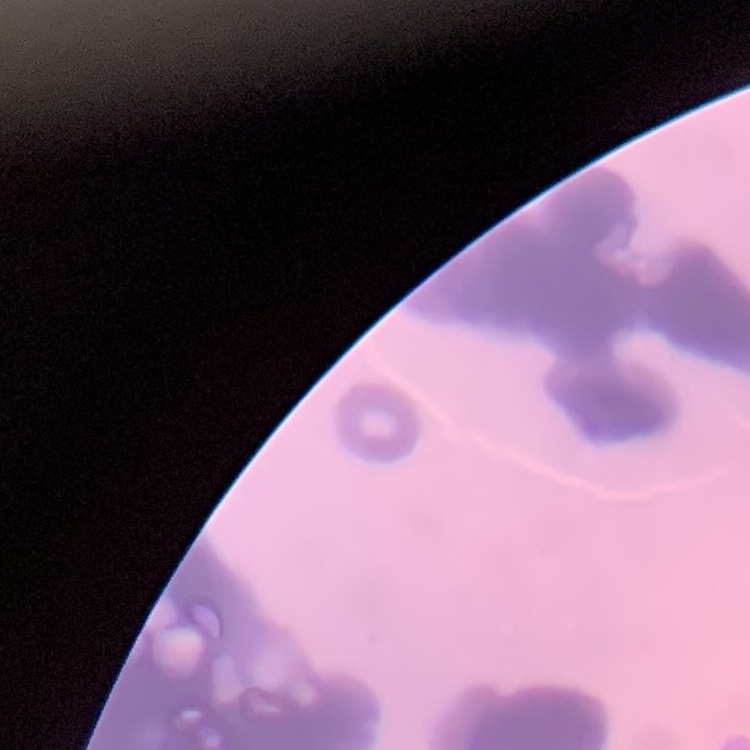

Summary:
  - Red blood cell morphology: rouleaux formation
  - Stain: Field's or Giemsa
  - Preparation: thin blood smear
  - Image type: one tile cut from a larger photomicrograph